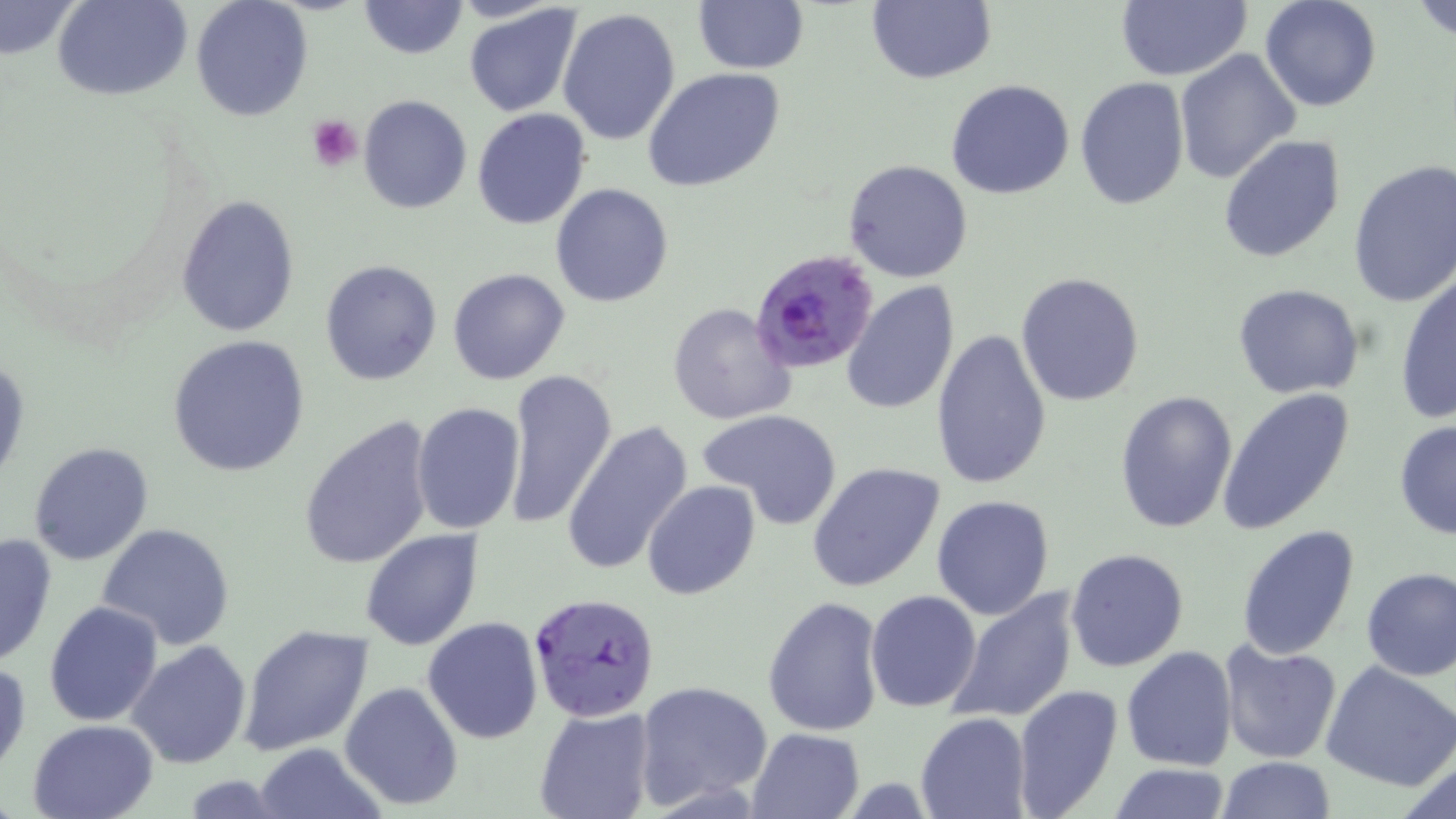
Plasmodium falciparum-infected red blood cell locations = approximate bounding boxes as (x1, y1, x2, y2) in pixels: (751, 249, 878, 374), (528, 591, 661, 723)
slide-level diagnosis = Plasmodium falciparum
preparation = thin blood smear
image size = 1456×819 pixels
field of view = single
uninfected red blood cell locations = approximate bounding boxes as (x1, y1, x2, y2) in pixels: (54, 0, 192, 100), (191, 0, 314, 121), (357, 0, 467, 59), (693, 0, 809, 73), (1259, 0, 1382, 112), (1409, 0, 1456, 44), (0, 1, 81, 63), (866, 1, 996, 85), (1116, 1, 1251, 81), (463, 4, 583, 117), (557, 7, 682, 146), (1172, 47, 1302, 184), (643, 68, 786, 193), (1076, 76, 1189, 211), (946, 79, 1076, 200), (358, 95, 472, 213), (472, 109, 591, 230), (1217, 134, 1347, 263), (842, 160, 973, 284), (1348, 160, 1456, 309), (551, 183, 674, 306), (177, 196, 299, 337), (320, 260, 441, 386), (447, 268, 570, 386), (1395, 270, 1455, 425), (1015, 272, 1145, 407), (841, 282, 960, 415), (1231, 283, 1364, 400), (668, 301, 799, 426), (931, 325, 1053, 489), (167, 336, 310, 477), (0, 353, 28, 489), (505, 368, 617, 528), (1216, 386, 1356, 535), (1114, 389, 1238, 533), (411, 402, 525, 536), (698, 408, 844, 529), (298, 414, 437, 571), (560, 418, 694, 577), (1393, 418, 1456, 542), (29, 442, 155, 566), (806, 460, 949, 595), (643, 481, 761, 601), (930, 494, 1056, 620), (97, 523, 236, 651), (1236, 524, 1361, 661), (361, 530, 482, 650), (0, 532, 58, 668), (1064, 548, 1189, 672), (1360, 566, 1456, 680), (948, 589, 1077, 723), (865, 590, 982, 712), (762, 596, 885, 736), (43, 599, 163, 727), (423, 617, 543, 742), (239, 625, 373, 757), (126, 639, 252, 769), (1218, 639, 1344, 765), (1120, 645, 1237, 771), (0, 660, 30, 776), (1321, 660, 1456, 791), (634, 679, 773, 809), (340, 681, 465, 810), (1012, 684, 1125, 819), (534, 706, 655, 819), (915, 711, 1033, 819), (27, 718, 157, 819), (746, 728, 865, 819), (252, 741, 384, 819), (1216, 756, 1336, 818), (1394, 759, 1456, 819), (1106, 762, 1234, 818)
platelet locations = approximate bounding boxes as (x1, y1, x2, y2) in pixels: (306, 115, 362, 169)
modality = light microscopy
stain = May-Grünwald-Giemsa
magnification = 1000x